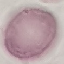

Result: negative for malaria parasites. Thin blood film. Acquired by smartphone through the microscope eyepiece. Giemsa-stained preparation. Cell patch, automatically extracted from a larger field of view and resized to 64 × 64 pixels.